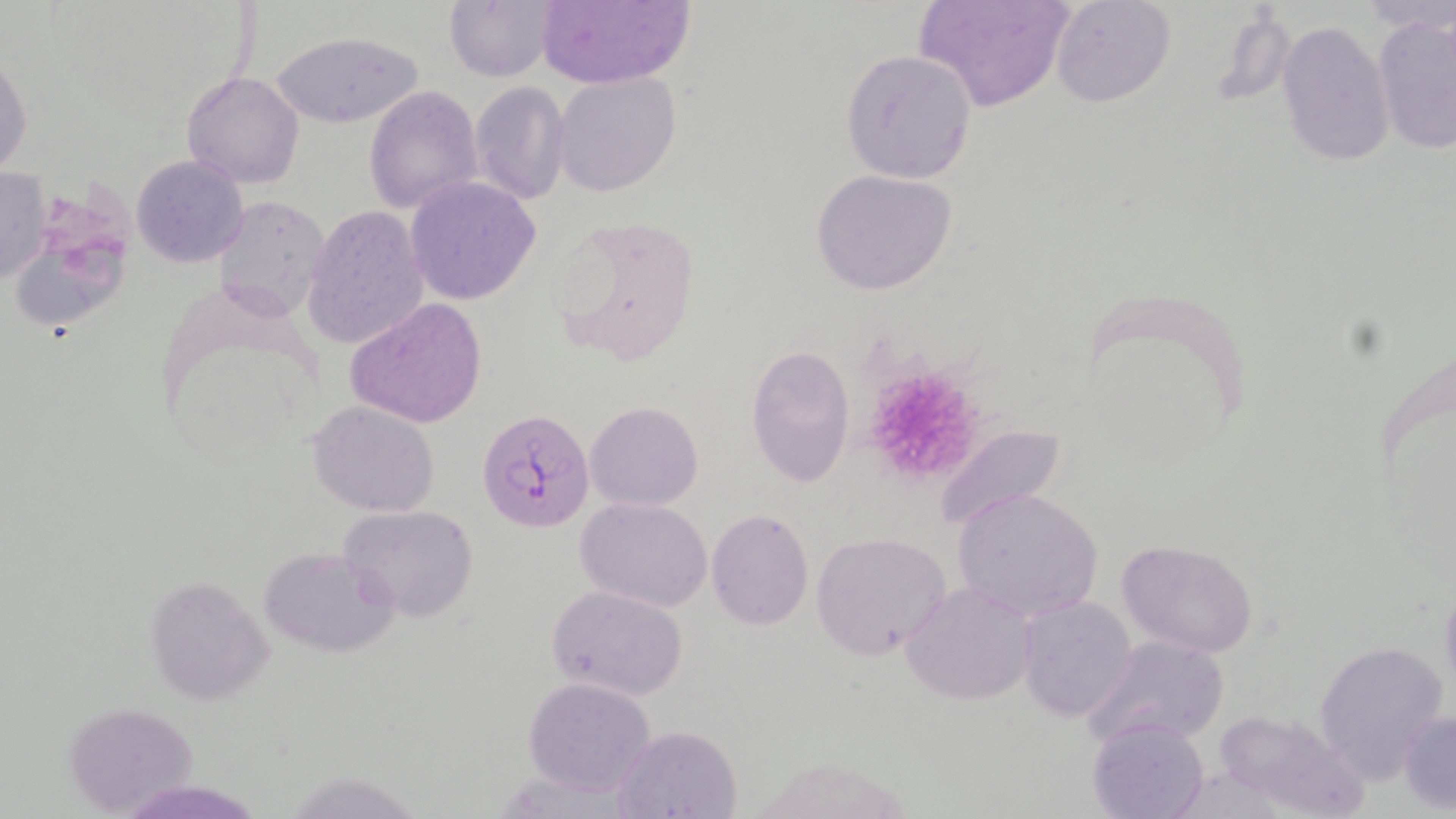

Summary:
  - Coordinate format: approximate bounding boxes as [x1, y1, x2, y2] in pixels
  - Uninfected red blood cell locations: [445, 0, 557, 82], [533, 0, 693, 89], [918, 0, 1073, 113], [1047, 0, 1175, 108], [1372, 14, 1455, 155], [1275, 20, 1393, 168], [268, 33, 425, 128], [1, 48, 32, 180], [841, 50, 977, 184], [180, 71, 305, 190], [552, 72, 681, 197], [471, 80, 570, 204], [365, 85, 482, 215], [130, 155, 250, 269], [0, 164, 51, 286], [811, 169, 957, 296], [405, 176, 543, 305], [211, 196, 334, 319], [301, 205, 430, 350], [551, 212, 700, 373], [17, 237, 131, 334], [346, 297, 486, 428], [745, 345, 855, 487], [307, 401, 440, 516], [585, 401, 704, 510], [932, 424, 1067, 533], [954, 488, 1104, 624], [576, 496, 714, 610], [339, 504, 478, 624], [706, 510, 814, 629], [810, 532, 953, 660], [1117, 538, 1259, 660], [257, 546, 401, 660], [147, 578, 273, 693], [903, 582, 1035, 706], [545, 584, 689, 700], [1017, 595, 1138, 723], [1084, 636, 1228, 752], [1312, 640, 1449, 777], [522, 676, 658, 797], [64, 701, 201, 814], [1213, 708, 1365, 819], [1399, 709, 1456, 812], [1090, 717, 1210, 819], [611, 725, 742, 817], [294, 774, 414, 819]
  - Plasmodium falciparum-infected red blood cell locations: [479, 409, 595, 535]
  - Platelet locations: [874, 369, 984, 477]
  - Slide-level diagnosis: Plasmodium falciparum
  - Stain: May-Grünwald-Giemsa
  - Field of view: one of a larger specimen
  - Image size: 1456×819 pixels
  - Magnification: 1000x
  - Preparation: thin blood film
  - Modality: optical microscopy